Locate every malaria parasite.
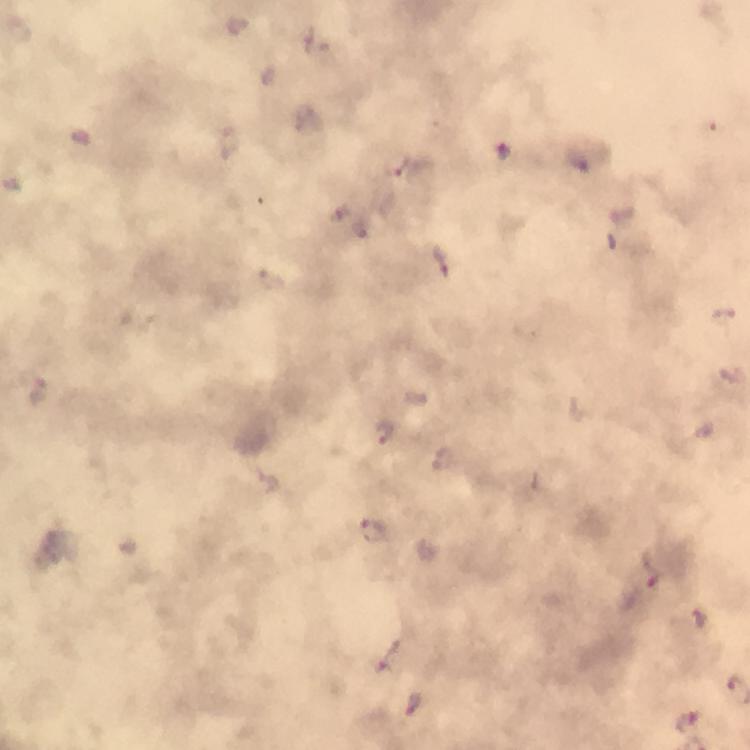

Approximate centers as {x, y} in pixels.
Malaria parasites: {505, 152}, {397, 165}, {442, 260}, {382, 434}, {375, 531}, {650, 568}, {700, 619}, {387, 657}, {414, 703}, {691, 722}.

Summary:
  - Preparation: thick blood smear
  - Context: from a malaria diagnostic workup
  - Cropped from: one field of view
  - Stain: Giemsa
  - Image size: 750×750 pixels
  - Immersion oil: used
  - Magnification: 100x
  - Capture: smartphone mounted on the microscope